Outline each blood parasite and name the species.
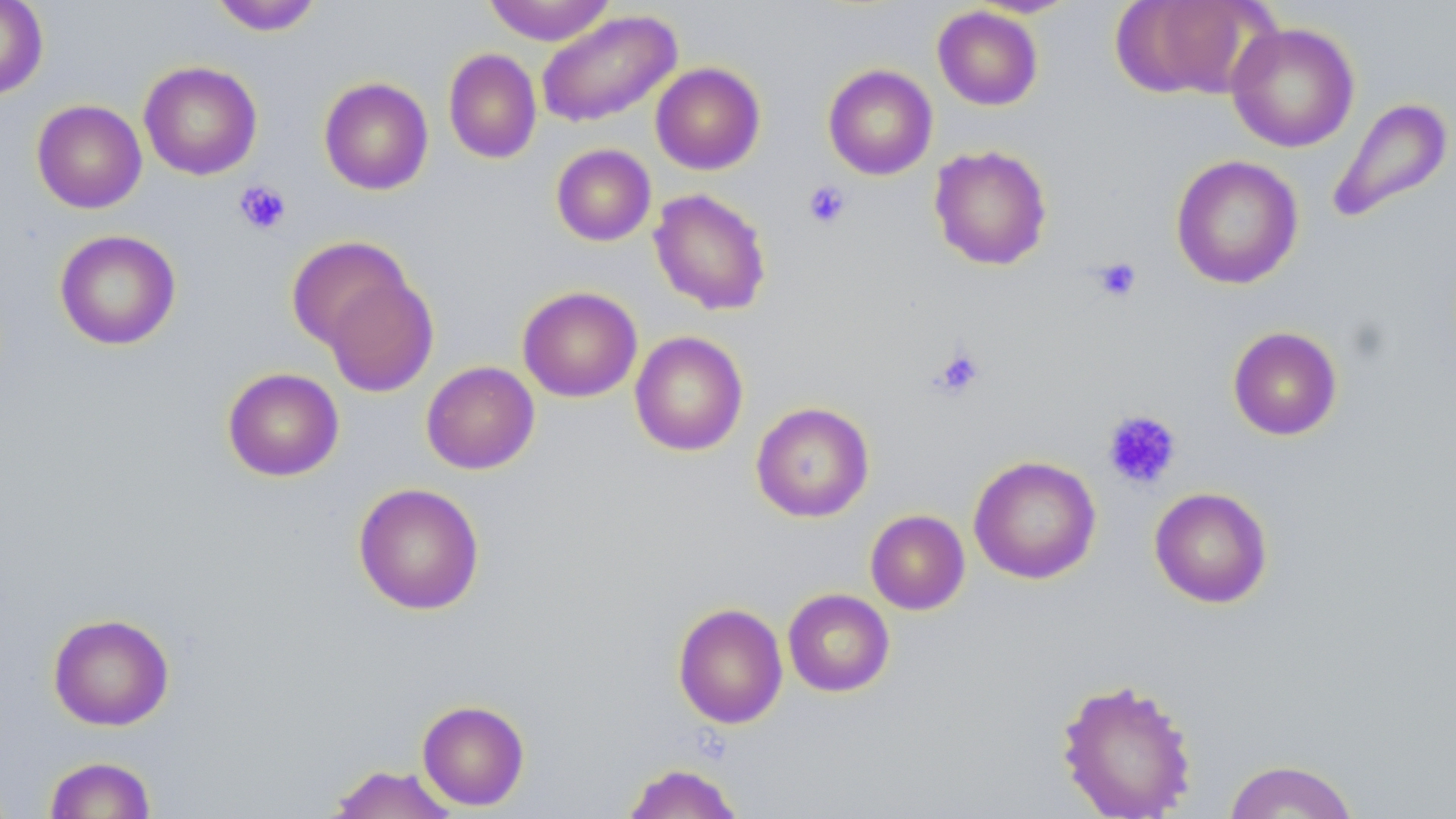

No blood parasites seen.

Approximate bounding boxes as [x1, y1, x2, y2] in pixels. Platelet locations: [234, 179, 291, 235], [803, 179, 852, 230], [1090, 257, 1143, 304], [930, 347, 985, 400], [1102, 410, 1183, 490]. Uninfected red blood cell locations: [0, 0, 48, 100], [209, 0, 324, 36], [484, 0, 615, 45], [1111, 0, 1265, 101], [932, 5, 1044, 110], [536, 9, 682, 128], [1226, 22, 1360, 153], [443, 48, 542, 164], [139, 60, 262, 180], [650, 62, 765, 175], [823, 64, 937, 180], [318, 77, 434, 195], [1327, 96, 1454, 226], [31, 99, 147, 213], [551, 143, 656, 246], [929, 144, 1053, 271], [1170, 155, 1304, 290], [648, 188, 772, 316], [54, 229, 181, 350], [286, 236, 413, 351], [320, 272, 438, 397], [517, 285, 642, 403], [1227, 326, 1343, 441], [629, 331, 748, 456], [421, 361, 540, 475], [222, 367, 344, 482], [750, 402, 874, 523], [968, 455, 1101, 584], [353, 482, 485, 615], [1149, 487, 1273, 608], [865, 509, 970, 615], [782, 588, 895, 697], [672, 602, 788, 729], [47, 612, 175, 731], [1055, 676, 1198, 819], [417, 700, 530, 811], [43, 755, 156, 818], [1222, 759, 1361, 818], [621, 762, 745, 818], [325, 764, 459, 819]. Slide-level diagnosis: negative for blood parasites. May-Grünwald-Giemsa-stained preparation. 1000x magnification. Single field of view. Thin blood film. Light microscopy. Image is 1456×819 pixels.